Identify the parasite.
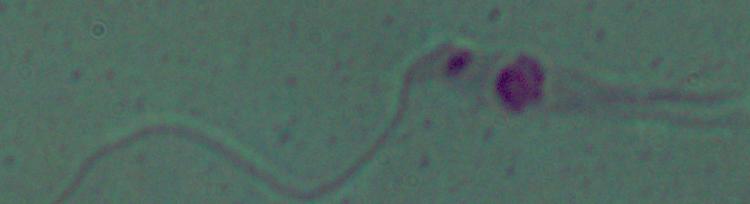

Leishmania.

modality: photomicrograph
magnification: 1000x